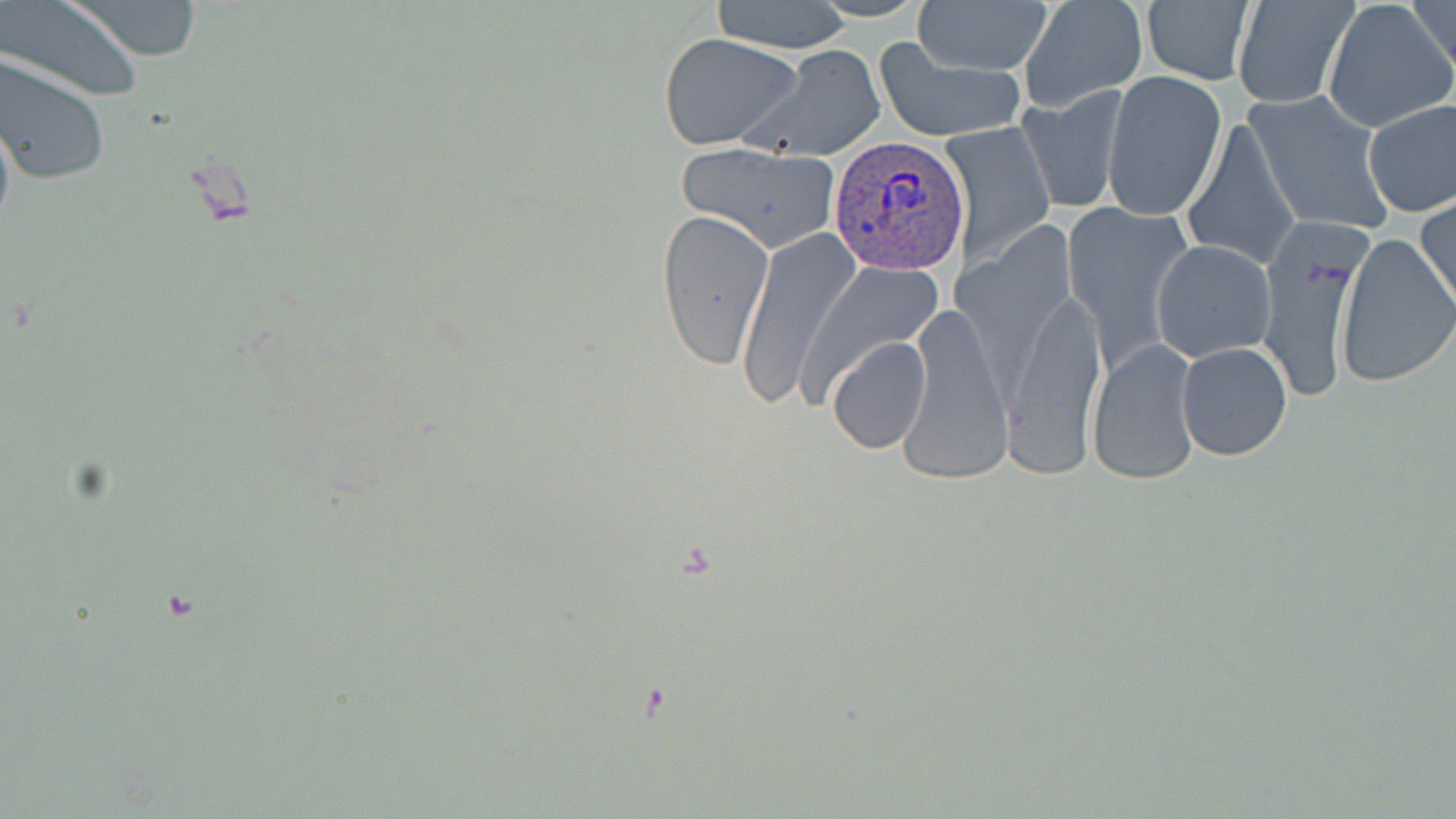

Summary:
  - Coordinate format: approximate bounding boxes as (x1,y1)-(x2,y2) corner pairs in pixels
  - Plasmodium vivax-infected red blood cell locations: (826,137)-(968,277)
  - Uninfected red blood cell locations: (1,0)-(147,102), (65,0)-(205,61), (711,0)-(855,53), (913,0)-(1051,77), (1019,0)-(1149,112), (1231,0)-(1359,109), (1324,0)-(1456,133), (1405,0)-(1456,81), (1140,2)-(1256,86), (659,32)-(803,151), (874,41)-(1027,143), (740,46)-(886,160), (0,54)-(110,186), (1102,69)-(1227,221), (1017,87)-(1128,214), (1244,89)-(1396,237), (1362,99)-(1456,217), (0,103)-(16,239), (1181,116)-(1300,272), (942,123)-(1057,265), (672,141)-(844,252), (1417,193)-(1456,315), (1063,200)-(1193,373), (654,209)-(773,369), (1254,224)-(1371,403), (734,229)-(857,407), (1335,231)-(1455,389), (1151,239)-(1278,362), (996,280)-(1109,480), (900,304)-(1012,481), (826,336)-(931,454), (1089,340)-(1201,486), (1175,342)-(1292,462)
  - Slide-level diagnosis: Plasmodium vivax
  - Magnification: 1000x
  - Stain: May-Grünwald-Giemsa
  - Modality: light microscopy
  - Field of view: one of a larger specimen
  - Image size: 1456×819 pixels
  - Preparation: thin blood film